Point out each leukocyte.
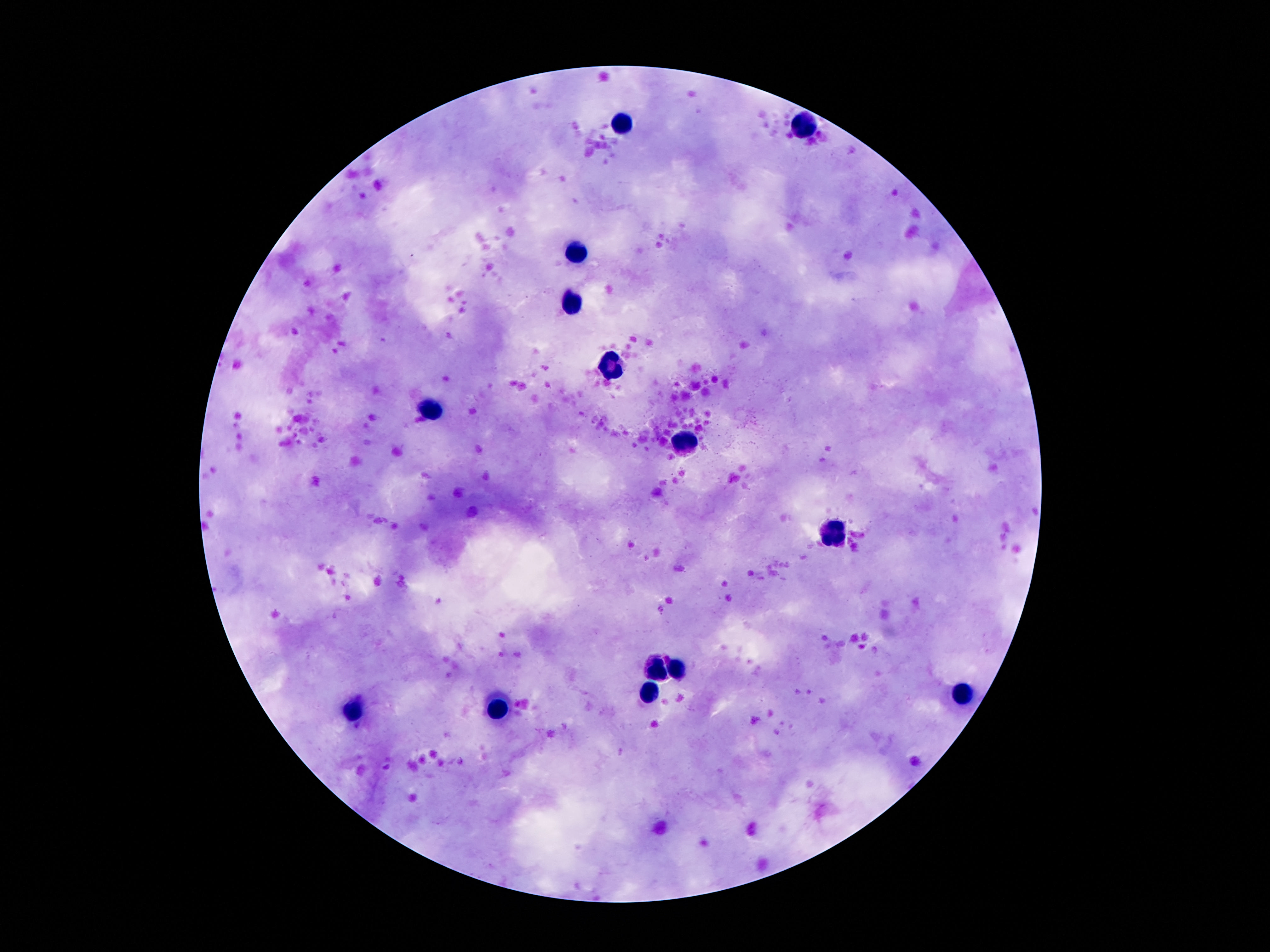
Approximate centers as (x, y) in pixels.
Leukocytes: (625, 124), (804, 124), (577, 251), (571, 302), (609, 367), (428, 411), (688, 445), (833, 535), (659, 668), (682, 668), (646, 693), (964, 697), (499, 711), (354, 712).

Thick peripheral-blood smear. Giemsa stain. Smartphone photograph taken through the microscope eyepiece. Patient malaria status: not infected. Image is 1270×952 pixels. One field from this slide. 100x magnification.